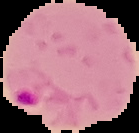
From a thin blood smear. Malaria status: parasitized. Image is 139×133 pixels. Segmented cell region on a black background.